Locate every leukocyte (white blood cell).
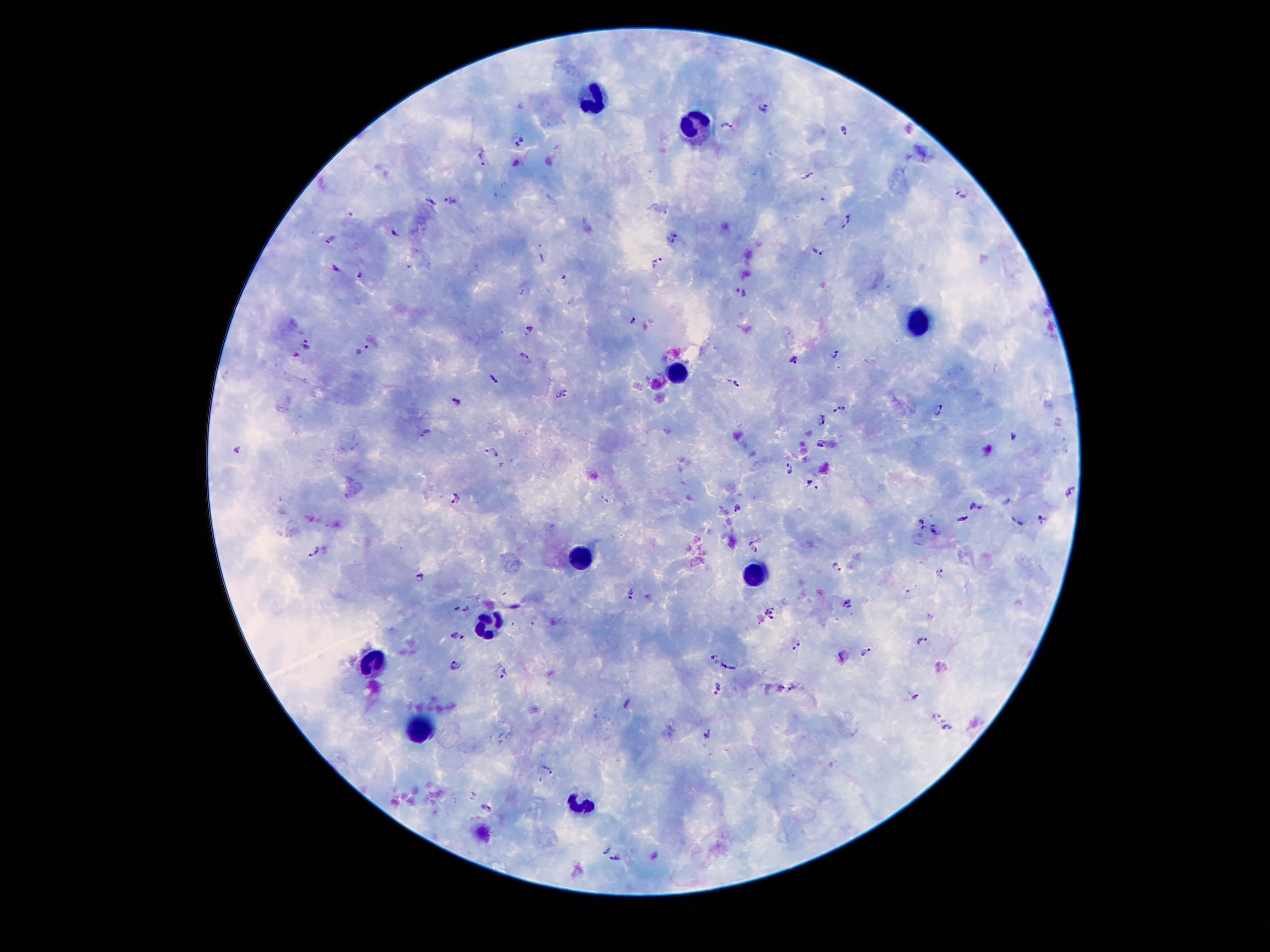
Approximate object centers, in pixels from the top-left corner.
Leukocytes: (x=597, y=100), (x=695, y=125), (x=923, y=318), (x=678, y=375), (x=584, y=556), (x=759, y=573), (x=490, y=622), (x=368, y=663), (x=424, y=733), (x=588, y=803).

Summary:
  - Plasmodium parasite locations: (x=764, y=107), (x=728, y=125), (x=845, y=129), (x=520, y=140), (x=481, y=157), (x=515, y=163), (x=807, y=176), (x=962, y=190), (x=450, y=199), (x=431, y=201), (x=846, y=221), (x=395, y=233), (x=673, y=238), (x=330, y=240), (x=818, y=254), (x=657, y=262), (x=335, y=269), (x=360, y=276), (x=564, y=280), (x=741, y=292), (x=526, y=293), (x=634, y=320), (x=530, y=329), (x=306, y=343), (x=364, y=350), (x=834, y=354), (x=526, y=355), (x=794, y=360), (x=493, y=379), (x=735, y=384), (x=563, y=395), (x=458, y=402), (x=839, y=410), (x=939, y=411), (x=824, y=421), (x=426, y=433), (x=1014, y=437), (x=820, y=446), (x=237, y=450), (x=494, y=451), (x=791, y=470), (x=811, y=483), (x=1071, y=493), (x=456, y=497), (x=1007, y=502), (x=977, y=507), (x=737, y=508), (x=965, y=518), (x=1016, y=520), (x=1040, y=520), (x=921, y=522), (x=935, y=531), (x=755, y=546), (x=316, y=551), (x=838, y=568), (x=941, y=572), (x=419, y=576), (x=629, y=594), (x=847, y=605), (x=461, y=609), (x=771, y=612), (x=458, y=636), (x=923, y=640), (x=797, y=644), (x=844, y=656), (x=712, y=657), (x=454, y=665), (x=729, y=666), (x=501, y=670), (x=778, y=687), (x=794, y=687), (x=720, y=689), (x=915, y=696), (x=628, y=703), (x=937, y=716), (x=947, y=729), (x=708, y=734), (x=549, y=769), (x=472, y=795), (x=486, y=807), (x=604, y=851), (x=615, y=859)
  - Stain: Giemsa
  - Patient malaria status: positive for Plasmodium falciparum
  - Image size: 1270×952 pixels
  - Magnification: 100x
  - Field of view: one from this slide
  - Capture: smartphone camera through the microscope eyepiece
  - Preparation: thick blood film